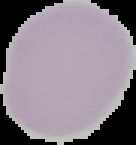

Cell region segmented out of the field of view; the surrounding area is masked to black. From a thin blood film. Image is 136×145 pixels. Result: no Plasmodium parasites seen.